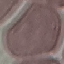

Summary:
  - Malaria status: uninfected
  - Capture: smartphone through the microscope eyepiece
  - Preparation: thin blood film
  - Image type: cell patch, automatically extracted from a larger field of view and resized to 64 × 64 pixels
  - Stain: Giemsa